Describe the morphology of the erythrocytes.
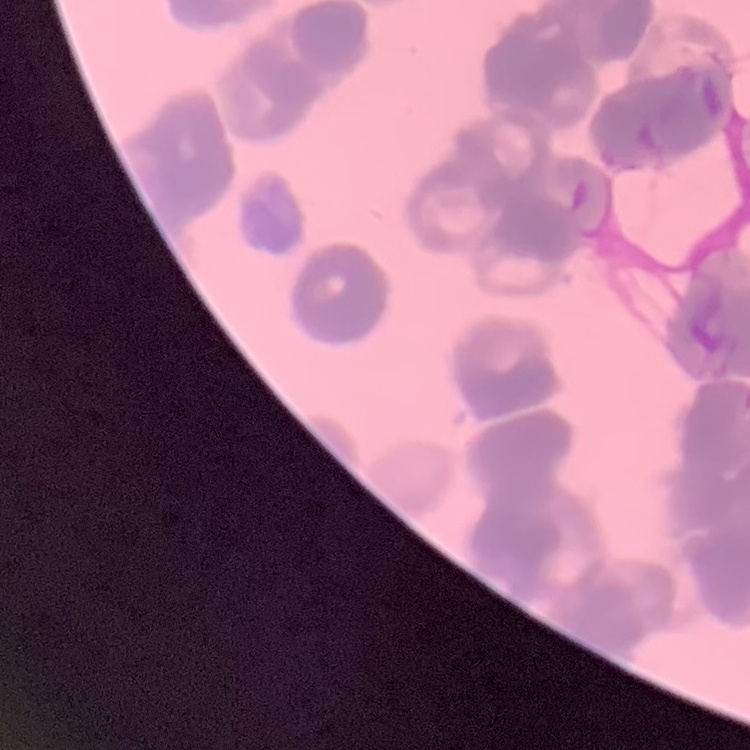
They show rouleaux formation.

Summary:
  - Image type: one tile cut from a larger photomicrograph
  - Stain: Field's or Giemsa
  - Preparation: thin peripheral smear